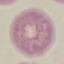
Summary:
  - Result: no malaria parasites seen
  - Preparation: thin blood smear
  - Capture: smartphone through the microscope eyepiece
  - Image type: automatically extracted cell patch, resized to 64 × 64 pixels
  - Stain: Giemsa